Assess this cell for malaria.
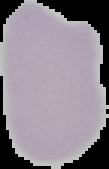
Uninfected.

From a thin blood film. The area outside the segmented cell region is set to black. Image is 109×169 pixels.